Classify this cell by malaria status.
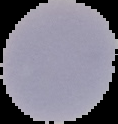

Uninfected.

From a thin blood smear. Image is 118×124 pixels. Segmented cell region on a black background.